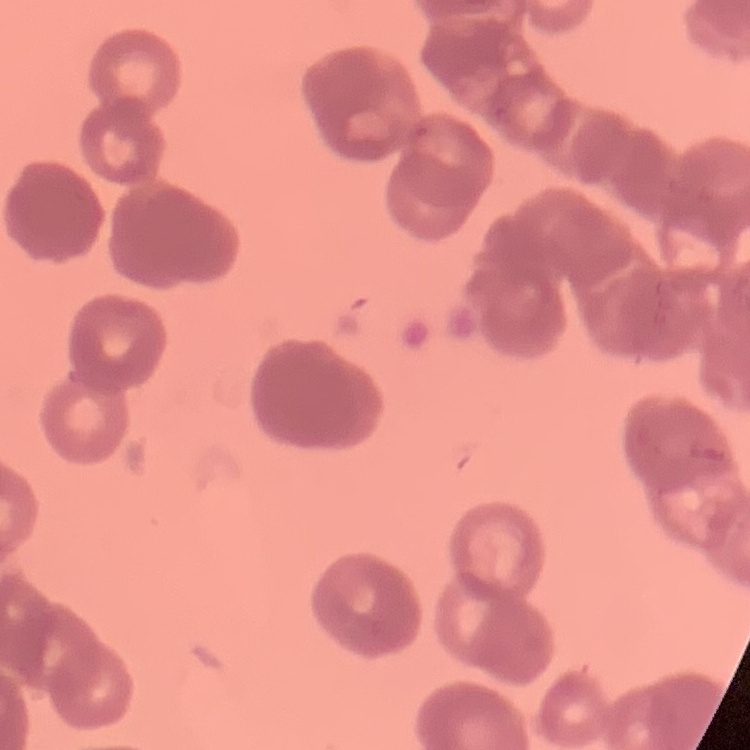

Summary:
  - Erythrocyte morphology: rouleaux formation
  - Stain: Field's or Giemsa
  - Image type: square crop of a larger photomicrograph
  - Preparation: thin blood film